Assess the morphology of the red blood cells.
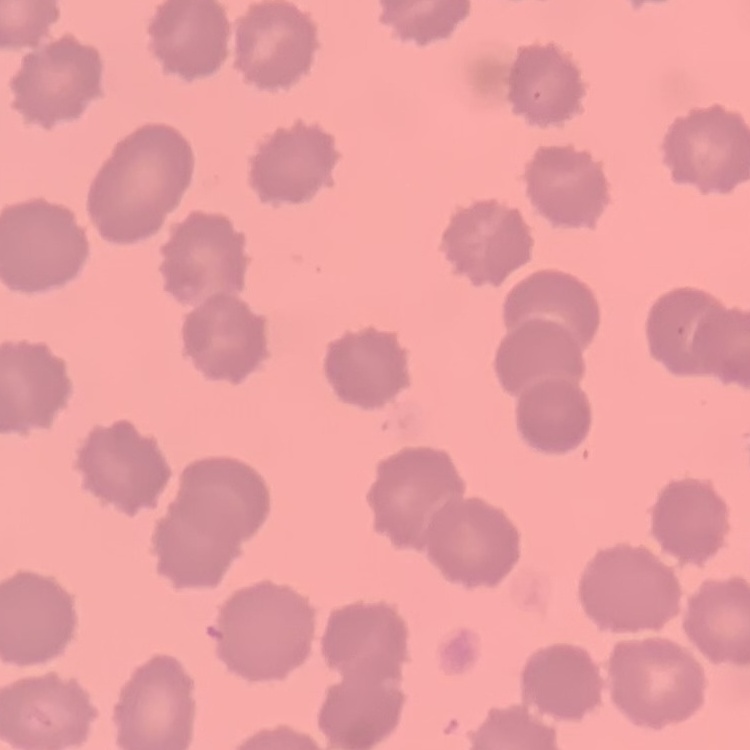
No rouleaux formation.

Thin blood smear. Stained with either Field's or Giemsa. One tile cut from a larger photomicrograph.